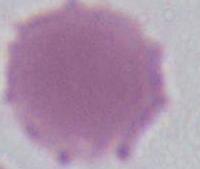

Summary:
  - Modality: micrograph
  - Identification: red blood cell
  - Magnification: 1000x